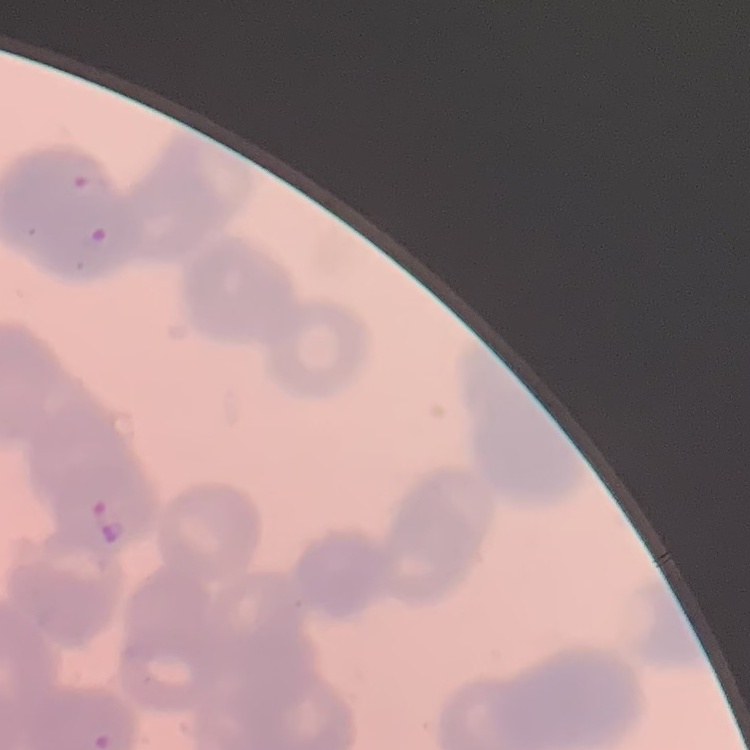

Summary:
  - Erythrocyte morphology: rouleaux formation
  - Image type: square crop of a larger photomicrograph
  - Preparation: thin peripheral smear
  - Stain: Field's or Giemsa